Identify the parasite.
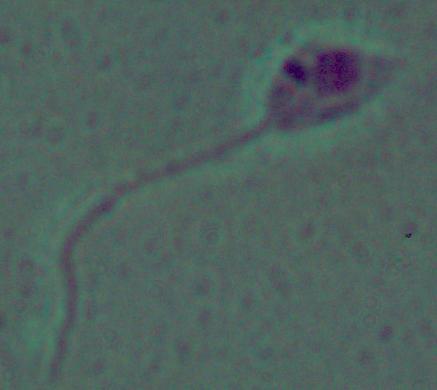
Leishmania.

modality = micrograph
magnification = 1000x